Outline each uninfected red blood cell.
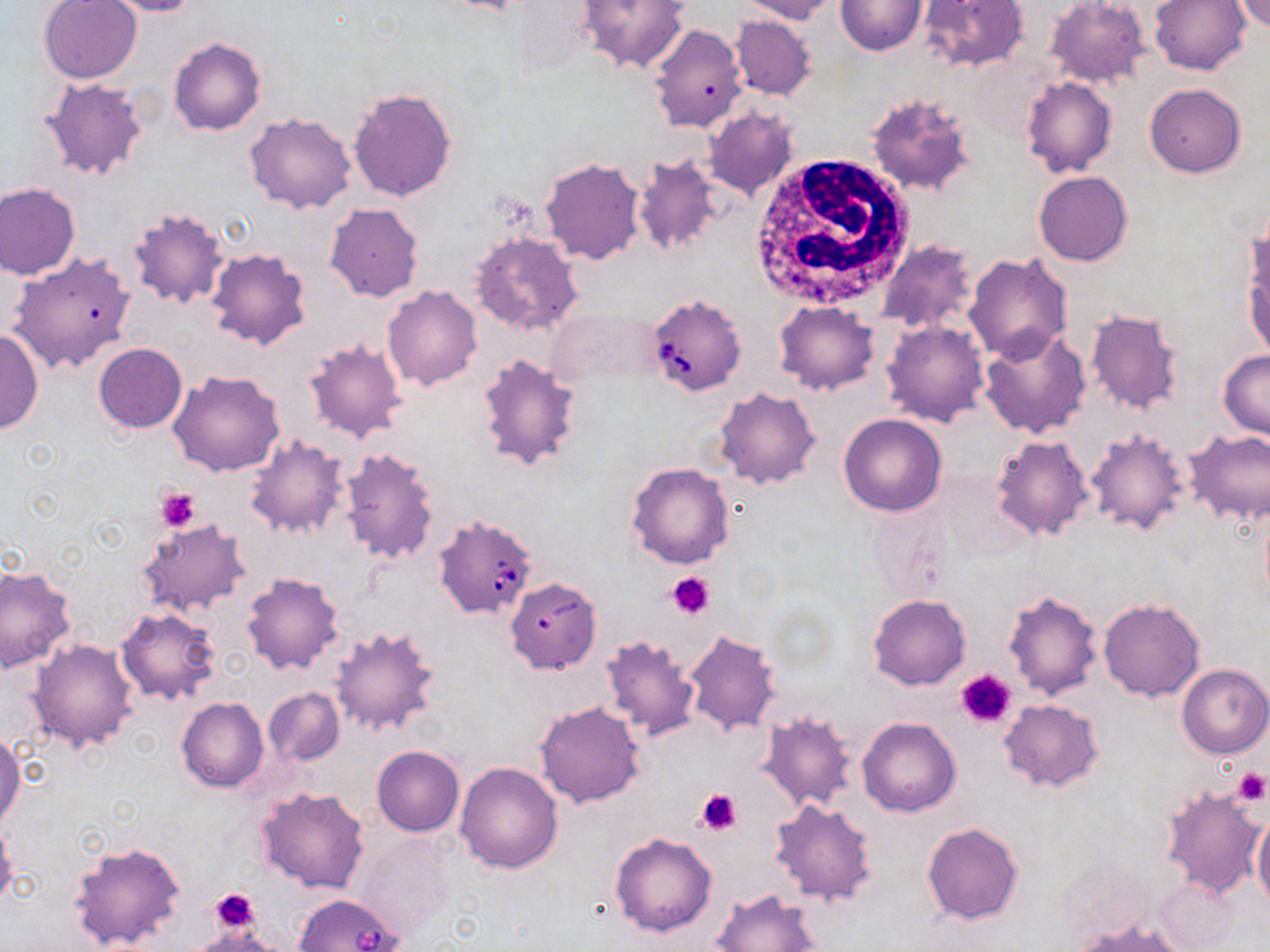
Approximate bounding boxes as (x1,y1)-(x2,y2) corner pairs in pixels.
Uninfected red blood cells: (38,0)-(142,84), (98,0)-(203,17), (577,0)-(690,74), (737,0)-(839,23), (836,0)-(927,54), (918,0)-(1029,72), (1044,0)-(1150,88), (1150,0)-(1251,75), (1233,1)-(1270,32), (730,14)-(817,101), (648,22)-(748,132), (168,37)-(265,135), (1021,76)-(1117,178), (38,77)-(150,182), (1145,84)-(1246,178), (349,88)-(458,202), (865,92)-(977,197), (704,106)-(799,201), (245,112)-(357,215), (631,153)-(726,257), (540,158)-(645,265), (1035,171)-(1132,266), (0,182)-(81,279), (324,202)-(423,302), (127,207)-(229,308), (469,231)-(584,338), (1243,236)-(1270,361), (875,241)-(981,337), (207,246)-(313,351), (7,251)-(137,374), (964,253)-(1073,364), (383,284)-(483,391), (773,302)-(880,395), (1085,306)-(1186,415), (548,307)-(662,390), (882,319)-(990,427), (0,326)-(44,434), (978,328)-(1091,439), (304,335)-(408,445), (94,343)-(186,433), (1219,349)-(1269,439), (477,353)-(583,472), (169,369)-(286,476), (715,387)-(821,490), (838,413)-(948,516), (1085,428)-(1191,537), (1183,429)-(1270,526), (243,434)-(350,539), (992,435)-(1092,539), (338,444)-(442,565), (626,461)-(733,569), (136,518)-(252,618), (0,566)-(76,674), (240,572)-(344,675), (1004,588)-(1104,701), (869,593)-(969,690), (1098,598)-(1205,701), (115,607)-(221,705), (329,623)-(441,738), (682,630)-(781,738), (598,635)-(702,740), (29,639)-(139,752), (1177,664)-(1270,758), (263,687)-(345,766), (177,697)-(269,791), (999,698)-(1104,791), (535,700)-(647,808), (756,710)-(859,813), (857,716)-(960,817), (0,732)-(23,831), (371,745)-(464,836), (455,762)-(564,873), (1159,781)-(1268,901), (256,786)-(371,895), (769,798)-(877,905), (1252,810)-(1270,911), (0,820)-(18,909), (922,821)-(1024,927), (609,833)-(718,937), (357,834)-(455,941), (69,840)-(187,952), (1153,874)-(1244,952), (714,888)-(824,952), (1074,918)-(1190,952).

Babesia divergens-infected red blood cell locations: (646,292)-(747,397), (433,515)-(537,620), (504,576)-(601,675), (292,893)-(404,951). Platelet locations: (157,488)-(199,531), (668,572)-(716,619), (955,669)-(1019,728), (1230,767)-(1268,806), (696,787)-(743,835), (206,888)-(260,935). White blood cell locations: (753,158)-(913,308). Slide-level diagnosis: Babesia divergens. May-Grünwald-Giemsa-stained preparation. Image is 1270×952 pixels. Thin blood smear. 1000x magnification. Single field of view. Light microscopy.